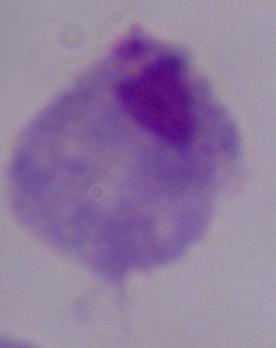
Summary:
  - Magnification: 1000x
  - Modality: photomicrograph
  - Identification: trichomonad